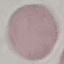 Result: no malaria parasites detected. Thin smear of blood. Giemsa-stained preparation. Acquired by smartphone through the microscope eyepiece. Automatically extracted cell patch, resized to 64 × 64 pixels.